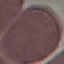
result = no malaria parasites detected
stain = Giemsa
preparation = thin smear
capture = smartphone through the microscope eyepiece
image type = cell patch, automatically extracted from a larger field of view and resized to 64 × 64 pixels